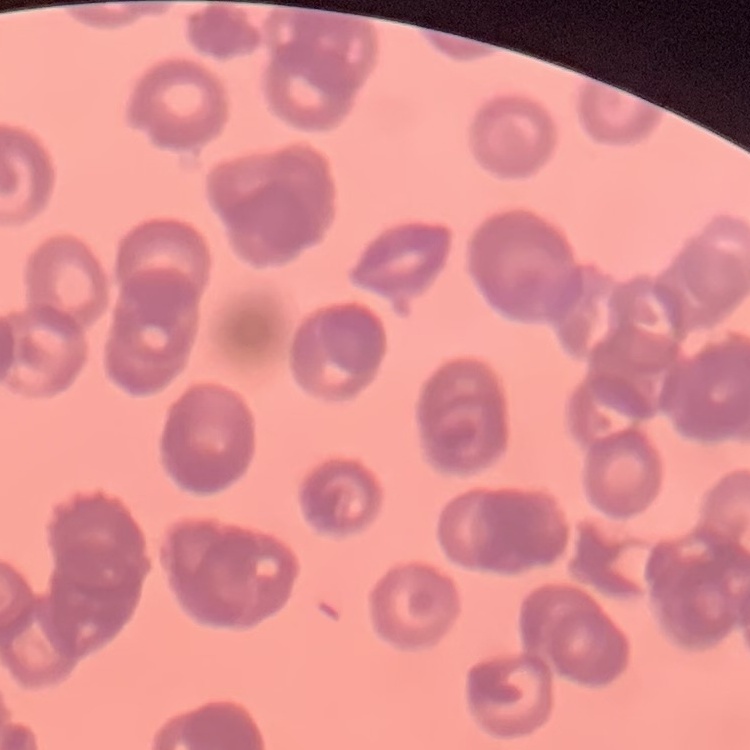

Summary:
  - Red blood cell morphology: rouleaux formation
  - Stain: Field's or Giemsa
  - Image type: square crop of a larger photomicrograph
  - Preparation: thin blood film